Identify the parasite.
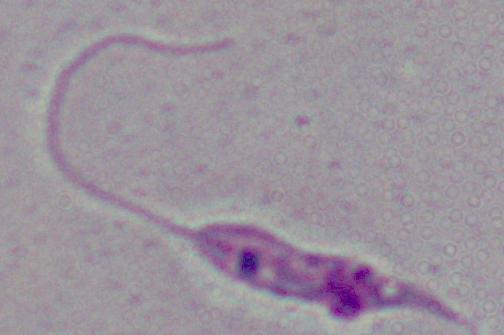
Leishmania.

magnification = 1000x
modality = photomicrograph